Classify this cell by malaria status.
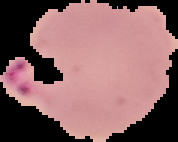
It is parasitized.

preparation = thin blood smear
image type = segmented cell region with the area outside set to black
image size = 178×142 pixels